Locate every blood parasite and identify its species.
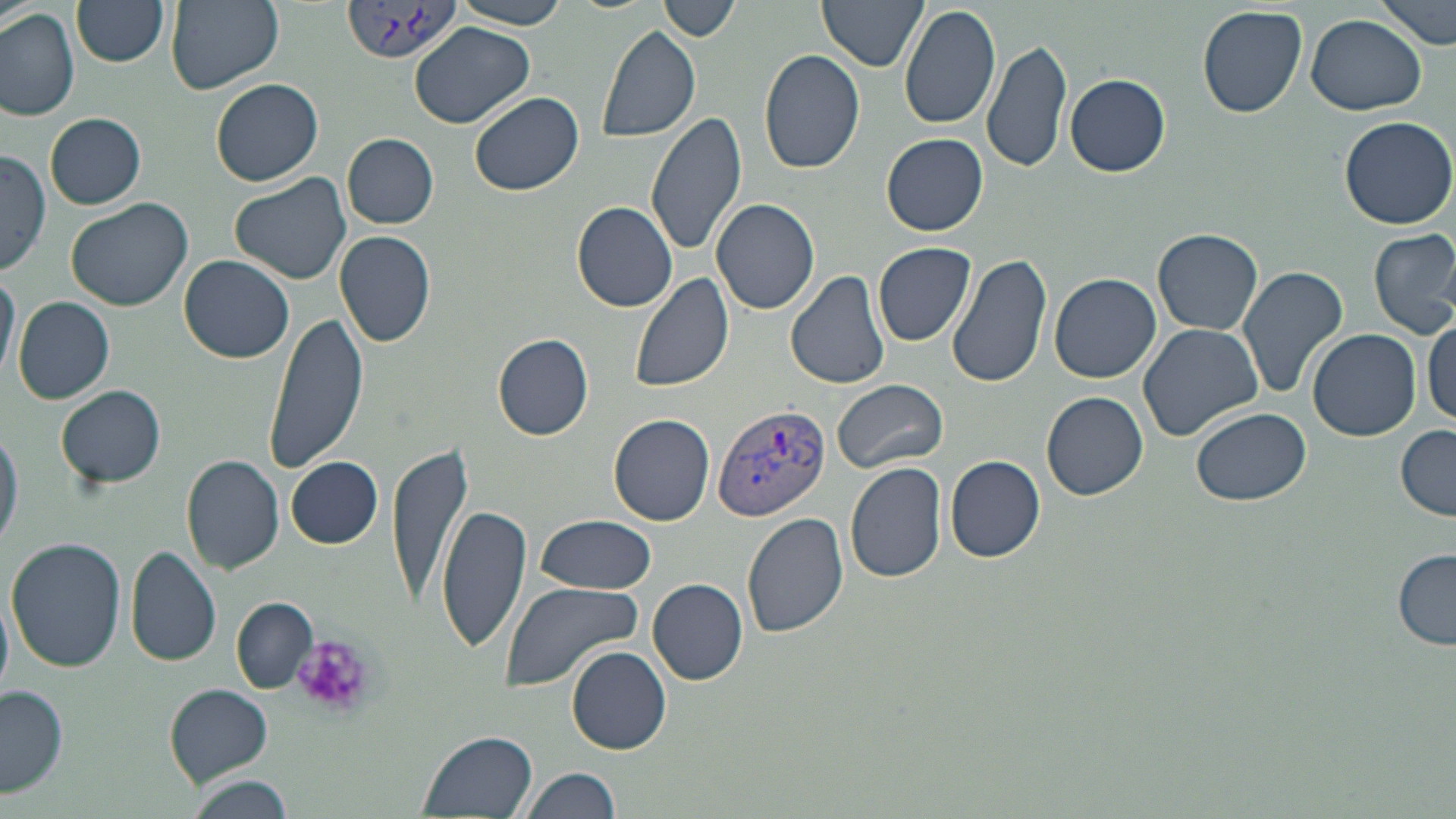
Approximate bounding boxes as named x1/y1/x2/y2 corners in pixels.
Plasmodium vivax-infected red blood cells: (x1=341, y1=3, x2=462, y2=67), (x1=712, y1=401, x2=832, y2=522).
No Plasmodium falciparum, Plasmodium ovale, Plasmodium malariae, Babesia divergens, or Trypanosoma brucei observed.

Platelet locations: (x1=293, y1=634, x2=375, y2=720). Uninfected red blood cell locations: (x1=71, y1=0, x2=170, y2=67), (x1=165, y1=0, x2=282, y2=92), (x1=658, y1=0, x2=740, y2=42), (x1=818, y1=0, x2=926, y2=71), (x1=1378, y1=0, x2=1453, y2=50), (x1=450, y1=1, x2=573, y2=29), (x1=900, y1=3, x2=1001, y2=131), (x1=1197, y1=5, x2=1307, y2=118), (x1=0, y1=8, x2=80, y2=121), (x1=1306, y1=15, x2=1425, y2=115), (x1=410, y1=22, x2=534, y2=127), (x1=594, y1=23, x2=702, y2=143), (x1=983, y1=35, x2=1073, y2=177), (x1=759, y1=48, x2=866, y2=175), (x1=1065, y1=73, x2=1170, y2=177), (x1=210, y1=76, x2=324, y2=187), (x1=469, y1=91, x2=582, y2=196), (x1=646, y1=107, x2=748, y2=258), (x1=45, y1=113, x2=146, y2=209), (x1=1338, y1=114, x2=1456, y2=229), (x1=343, y1=133, x2=438, y2=229), (x1=881, y1=133, x2=988, y2=235), (x1=0, y1=151, x2=50, y2=277), (x1=229, y1=174, x2=353, y2=284), (x1=66, y1=198, x2=195, y2=311), (x1=711, y1=198, x2=821, y2=316), (x1=572, y1=202, x2=677, y2=312), (x1=1153, y1=227, x2=1264, y2=335), (x1=1369, y1=228, x2=1456, y2=338), (x1=336, y1=231, x2=436, y2=346), (x1=874, y1=242, x2=976, y2=345), (x1=947, y1=252, x2=1053, y2=390), (x1=179, y1=255, x2=295, y2=363), (x1=0, y1=264, x2=20, y2=385), (x1=1236, y1=266, x2=1348, y2=400), (x1=629, y1=268, x2=736, y2=394), (x1=786, y1=270, x2=893, y2=390), (x1=1048, y1=272, x2=1162, y2=385), (x1=12, y1=295, x2=114, y2=406), (x1=265, y1=308, x2=368, y2=473), (x1=1424, y1=318, x2=1456, y2=429), (x1=1138, y1=322, x2=1265, y2=444), (x1=1307, y1=328, x2=1422, y2=441), (x1=495, y1=332, x2=594, y2=440), (x1=832, y1=378, x2=948, y2=474), (x1=57, y1=385, x2=166, y2=489), (x1=1042, y1=391, x2=1148, y2=500), (x1=1191, y1=406, x2=1310, y2=506), (x1=609, y1=413, x2=715, y2=526), (x1=1396, y1=421, x2=1454, y2=521), (x1=0, y1=424, x2=22, y2=553), (x1=386, y1=441, x2=474, y2=605), (x1=944, y1=454, x2=1045, y2=563), (x1=181, y1=455, x2=285, y2=574), (x1=286, y1=457, x2=383, y2=548), (x1=846, y1=461, x2=947, y2=584), (x1=437, y1=503, x2=531, y2=654), (x1=743, y1=512, x2=849, y2=639), (x1=533, y1=515, x2=658, y2=596), (x1=6, y1=536, x2=128, y2=671), (x1=126, y1=546, x2=222, y2=667), (x1=1393, y1=549, x2=1455, y2=650), (x1=647, y1=578, x2=747, y2=685), (x1=501, y1=579, x2=644, y2=692), (x1=232, y1=599, x2=317, y2=694), (x1=567, y1=644, x2=673, y2=755), (x1=1, y1=684, x2=69, y2=801), (x1=165, y1=685, x2=273, y2=784), (x1=417, y1=730, x2=538, y2=818), (x1=519, y1=766, x2=621, y2=819), (x1=183, y1=775, x2=296, y2=819). Slide-level diagnosis: Plasmodium vivax. 1000x magnification. Optical microscopy. One field of a larger specimen. Thin blood smear. Image is 1456×819 pixels. May-Grünwald-Giemsa stain.